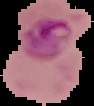 Segmented cell region on a black background. Image is 94×106 pixels. From a thin blood smear. Result: malaria parasites detected.